Report the malaria status of this cell.
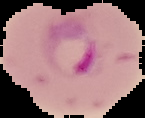

Parasitized.

preparation: thin blood smear
image_size: 145×118 pixels
image_type: cell region segmented out of the field of view; surrounding area masked to black